Assess the morphology of the erythrocytes.
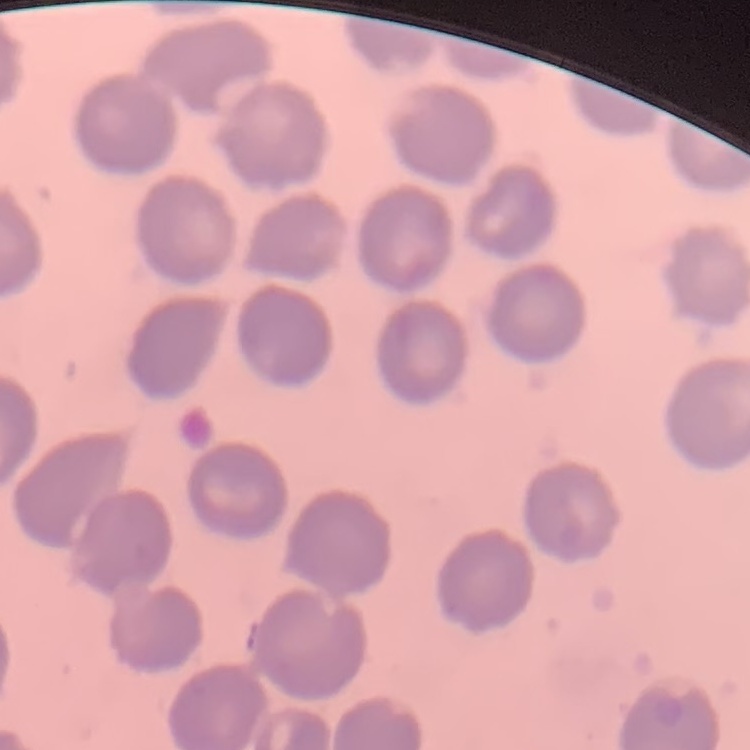
No rouleaux formation.

Summary:
  - Preparation: thin blood film
  - Stain: Field's or Giemsa
  - Image type: one tile cut from a larger photomicrograph